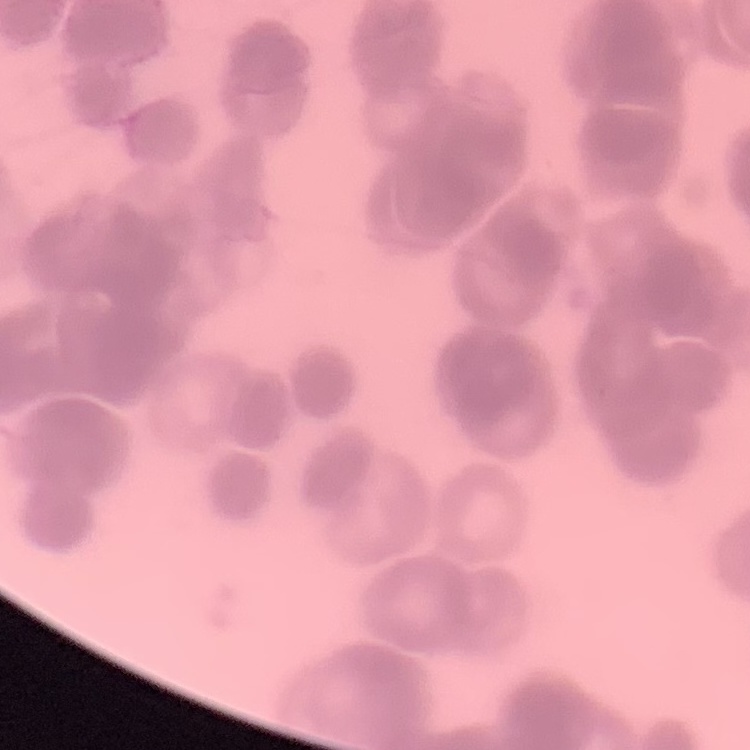

red blood cell morphology = rouleaux formation
stain = Field's or Giemsa
preparation = thin blood film
image type = square crop of a larger photomicrograph